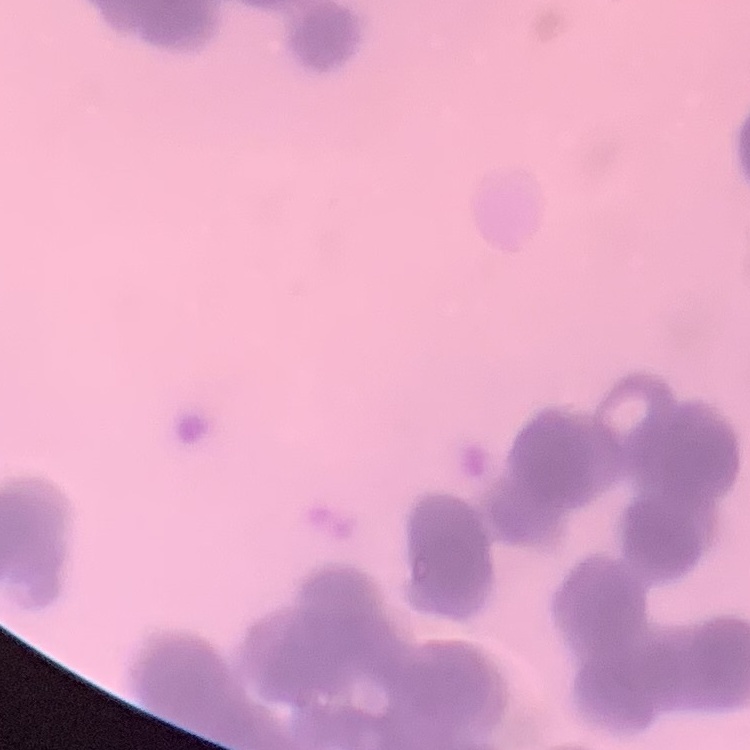
red_blood_cell_morphology: rouleaux formation
image_type: one tile cut from a larger photomicrograph
stain: Field's or Giemsa
preparation: thin blood smear